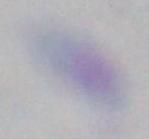
Summary:
  - Magnification: 1000x
  - Identification: Toxoplasma gondii
  - Modality: photomicrograph